Report the malaria status of this cell.
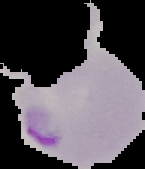
Parasitized.

Summary:
  - Preparation: thin blood smear
  - Image size: 145×169 pixels
  - Image type: cell region segmented out of the field of view; surrounding area masked to black